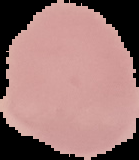 Image is 139×160 pixels. Result: no Plasmodium parasites seen. Segmented cell region on a black background. From a thin blood film.